Assess this cell for malaria.
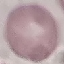
Uninfected.

Giemsa stain. Photographed with a smartphone camera at the microscope eyepiece. Thin smear of blood. Cell patch, automatically extracted from a larger field of view and resized to 64 × 64 pixels.